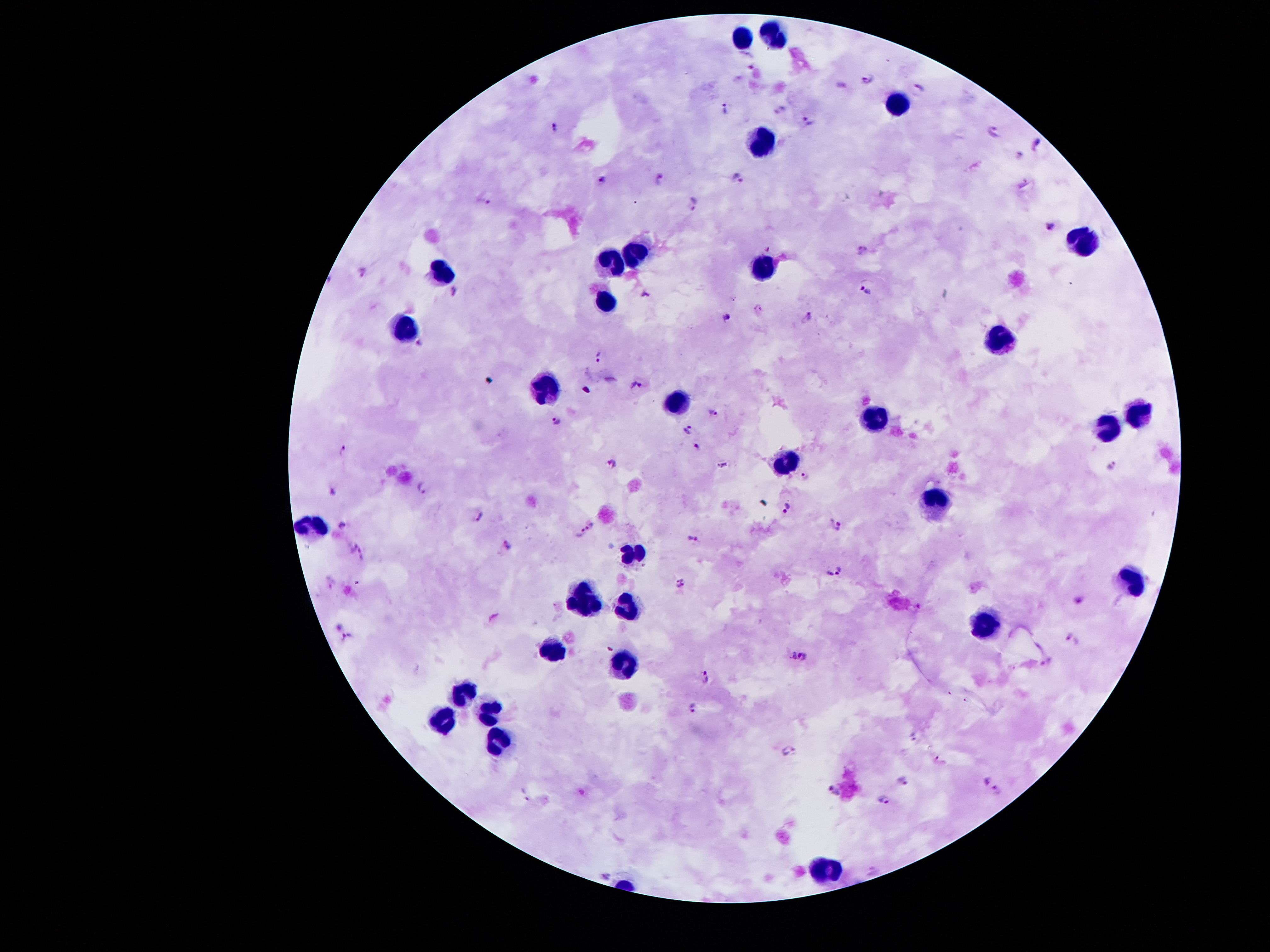

coordinate format = approximate centers as (x, y) in pixels
leukocyte locations = (739, 36), (771, 36), (894, 105), (763, 140), (1077, 239), (631, 253), (607, 261), (767, 268), (441, 271), (605, 300), (410, 329), (1000, 338), (551, 389), (679, 402), (1134, 409), (874, 418), (1107, 429), (784, 463), (931, 499), (319, 524), (633, 553), (1131, 579), (585, 599), (631, 605), (983, 626), (552, 651), (622, 663), (463, 696), (488, 716), (439, 725), (498, 743), (828, 865)
Plasmodium parasite locations = (753, 63), (869, 78), (842, 84), (919, 88), (726, 109), (779, 109), (809, 119), (555, 125), (995, 127), (1037, 144), (1020, 157), (662, 175), (603, 176), (735, 176), (483, 201), (693, 204), (1050, 224), (767, 247), (862, 250), (364, 269), (863, 287), (456, 291), (646, 293), (811, 314), (726, 315), (420, 342), (600, 357), (609, 382), (637, 384), (715, 413), (558, 419), (688, 429), (698, 446), (344, 448), (613, 463), (1111, 464), (723, 466), (807, 474), (422, 487), (333, 489), (785, 508), (478, 516), (343, 524), (836, 525), (593, 526), (581, 533), (693, 538), (352, 543), (508, 547), (364, 556), (836, 568), (332, 582), (680, 583), (1077, 600), (346, 637), (1072, 640), (804, 656), (793, 657), (1047, 662), (706, 678), (693, 706), (913, 735), (787, 752), (938, 757), (903, 780), (987, 781), (835, 789), (998, 790), (524, 794), (885, 798), (606, 876)
magnification = 100x
patient malaria status = infected with Plasmodium falciparum
capture = smartphone through the microscope eyepiece
field of view = one from this slide
image size = 1270×952 pixels
stain = Giemsa
preparation = thick blood film